Identify the parasite.
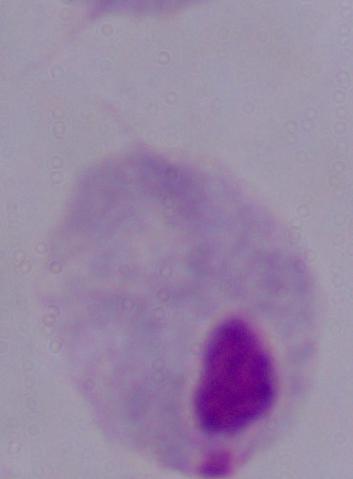
This is a trichomonad.

{
  "modality": "photomicrograph",
  "magnification": "1000x"
}